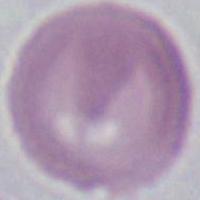

1000x magnification. Photomicrograph. A red blood cell is seen.